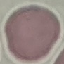

result = no malaria parasites detected
image type = cell patch, automatically extracted from a larger field of view and resized to 64 × 64 pixels
preparation = thin blood smear
capture = smartphone through the microscope eyepiece
stain = Giemsa